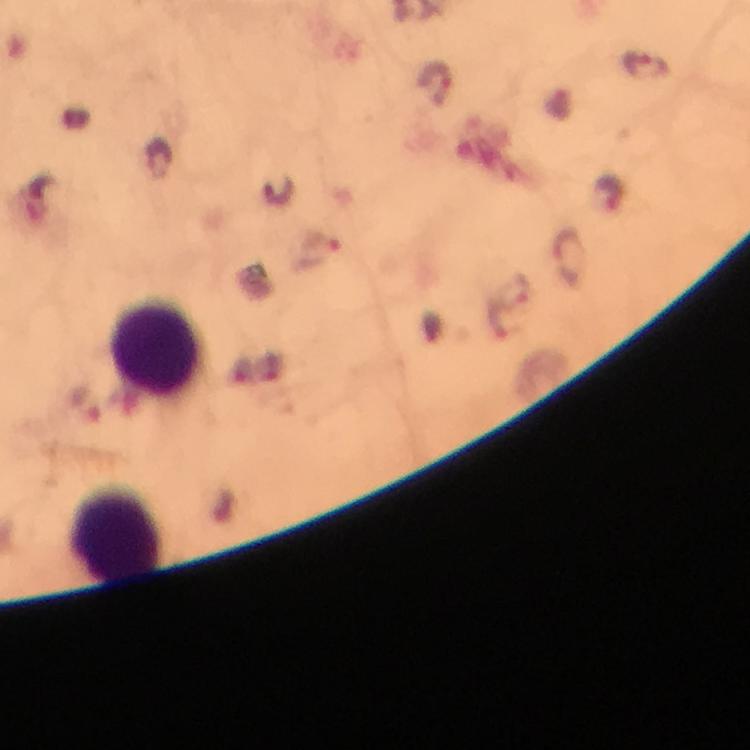

image size = 750×750 pixels
preparation = thick blood film
cropped from = a single field of view
context = from a diagnostic examination for malaria
stain = Giemsa
magnification = 100x
Plasmodium parasite locations = approximate object centers, in pixels from the top-left corner: (x=646, y=67), (x=437, y=83), (x=159, y=159), (x=279, y=193), (x=610, y=193), (x=323, y=247), (x=568, y=260), (x=517, y=292), (x=499, y=320)
capture = smartphone camera through the microscope
immersion oil = used
leukocyte locations = approximate object centers, in pixels from the top-left corner: (x=156, y=348), (x=114, y=533)